Locate every uninfected red blood cell.
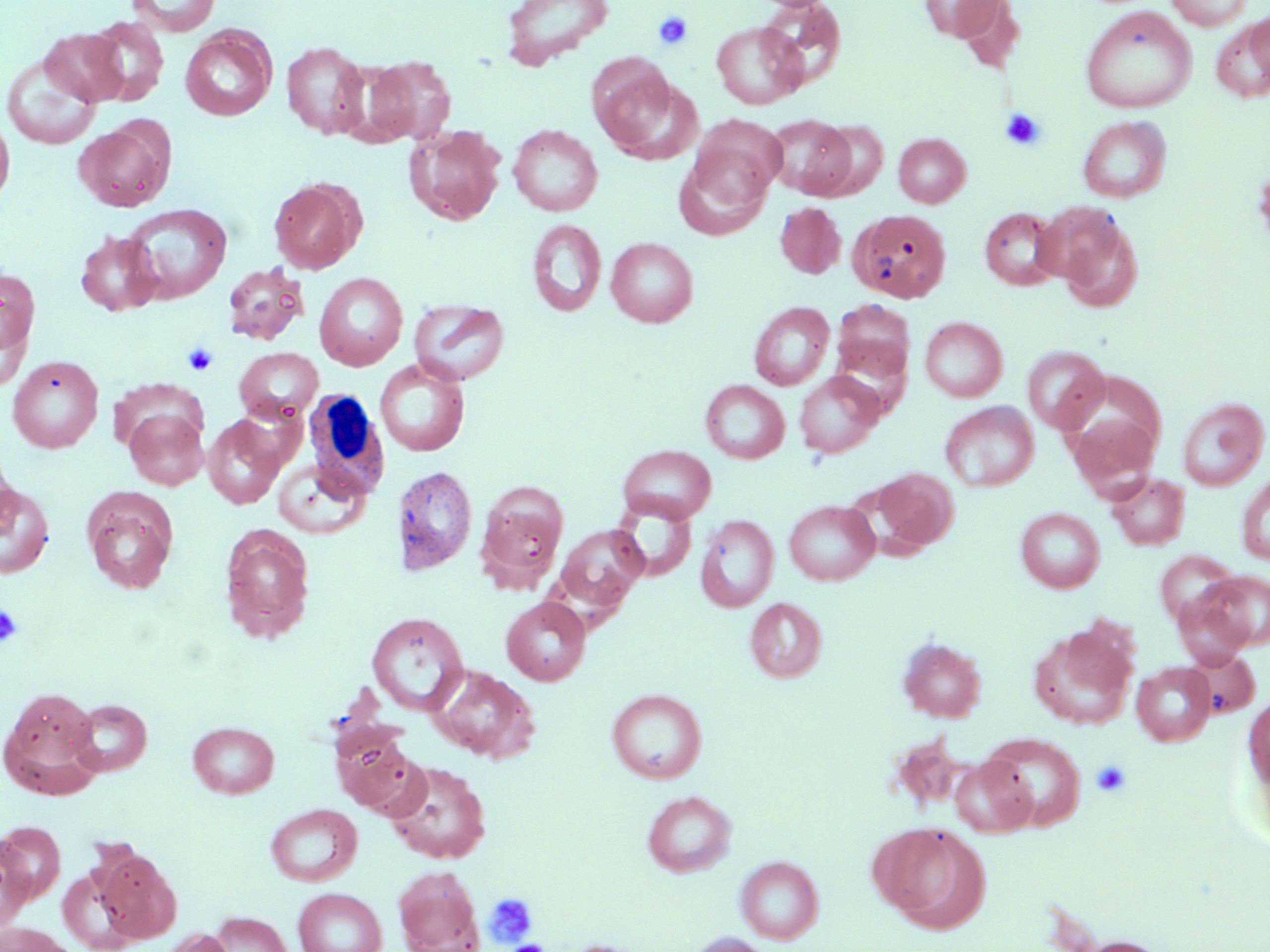
Approximate bounding boxes as (x1, y1, x2, y2) in pixels.
Uninfected red blood cells: (125, 0, 221, 36), (500, 0, 614, 69), (757, 0, 847, 89), (918, 0, 1007, 41), (953, 0, 1026, 75), (1166, 0, 1253, 31), (1080, 7, 1197, 114), (1247, 11, 1270, 85), (85, 17, 168, 106), (1212, 17, 1270, 101), (711, 21, 807, 109), (180, 27, 276, 121), (40, 28, 128, 105), (281, 40, 369, 139), (1, 53, 102, 150), (362, 55, 456, 145), (595, 67, 700, 164), (0, 111, 15, 210), (691, 114, 786, 199), (764, 114, 856, 198), (1078, 116, 1172, 202), (74, 119, 174, 211), (809, 119, 889, 200), (404, 124, 505, 225), (508, 125, 603, 216), (894, 132, 971, 207), (673, 145, 774, 240), (269, 178, 365, 274), (774, 202, 846, 279), (122, 203, 232, 303), (979, 207, 1064, 291), (849, 208, 952, 303), (1055, 214, 1143, 312), (527, 219, 607, 317), (75, 230, 163, 316), (606, 236, 699, 327), (222, 262, 309, 345), (0, 266, 40, 366), (314, 272, 408, 371), (409, 299, 510, 385), (832, 299, 915, 384), (749, 302, 835, 390), (920, 316, 1008, 402), (829, 336, 913, 417), (1022, 346, 1108, 434), (234, 347, 322, 422), (7, 355, 104, 453), (375, 358, 470, 457), (1058, 369, 1167, 472), (794, 372, 884, 458), (700, 379, 789, 464), (1177, 397, 1269, 491), (940, 401, 1039, 492), (124, 408, 208, 490), (1066, 409, 1160, 495), (202, 415, 286, 509), (617, 444, 717, 524), (0, 449, 18, 540), (272, 457, 373, 539), (391, 465, 478, 575), (871, 467, 959, 551), (1106, 472, 1190, 551), (1236, 473, 1270, 567), (0, 482, 54, 578), (475, 482, 568, 588), (82, 487, 180, 594), (609, 499, 698, 582), (784, 500, 880, 586), (1016, 507, 1104, 593), (695, 514, 779, 612), (554, 524, 649, 613), (219, 525, 316, 643), (1155, 550, 1242, 629), (1197, 570, 1270, 651), (1183, 574, 1264, 717), (1172, 592, 1252, 668), (501, 597, 591, 685), (745, 597, 826, 682), (367, 612, 469, 716), (1028, 626, 1136, 730), (897, 637, 987, 722), (1185, 649, 1260, 719), (1131, 661, 1216, 746), (430, 665, 539, 763), (1, 686, 105, 796), (606, 688, 707, 783), (1244, 692, 1270, 799), (69, 699, 152, 776), (187, 721, 279, 798), (331, 726, 418, 812), (982, 733, 1086, 830), (949, 755, 1037, 838), (385, 761, 491, 863), (642, 790, 736, 877), (265, 803, 362, 886), (877, 822, 990, 932), (0, 834, 36, 933), (93, 846, 181, 944), (736, 855, 824, 943), (393, 867, 484, 952), (292, 887, 387, 952), (207, 912, 294, 952), (0, 922, 79, 952), (159, 928, 236, 952), (686, 933, 777, 952), (1070, 936, 1174, 952), (562, 939, 649, 952).

slide_level_diagnosis: negative for blood parasites
field_of_view: one of a larger specimen
magnification: 1000x
stain: May-Grünwald-Giemsa
white_blood_cell_locations: 'approximate bounding boxes as (x1, y1, x2, y2) in pixels: (302, 390, 388, 499)'
modality: optical microscopy
preparation: thin blood film
platelet_locations: 'approximate bounding boxes as (x1, y1, x2, y2) in pixels: (653, 10, 693, 51), (1000, 108, 1047, 151), (182, 343, 219, 376), (0, 604, 23, 648), (1091, 759, 1132, 798), (484, 893, 539, 947), (502, 941, 552, 952)'
image_size: 1270×952 pixels